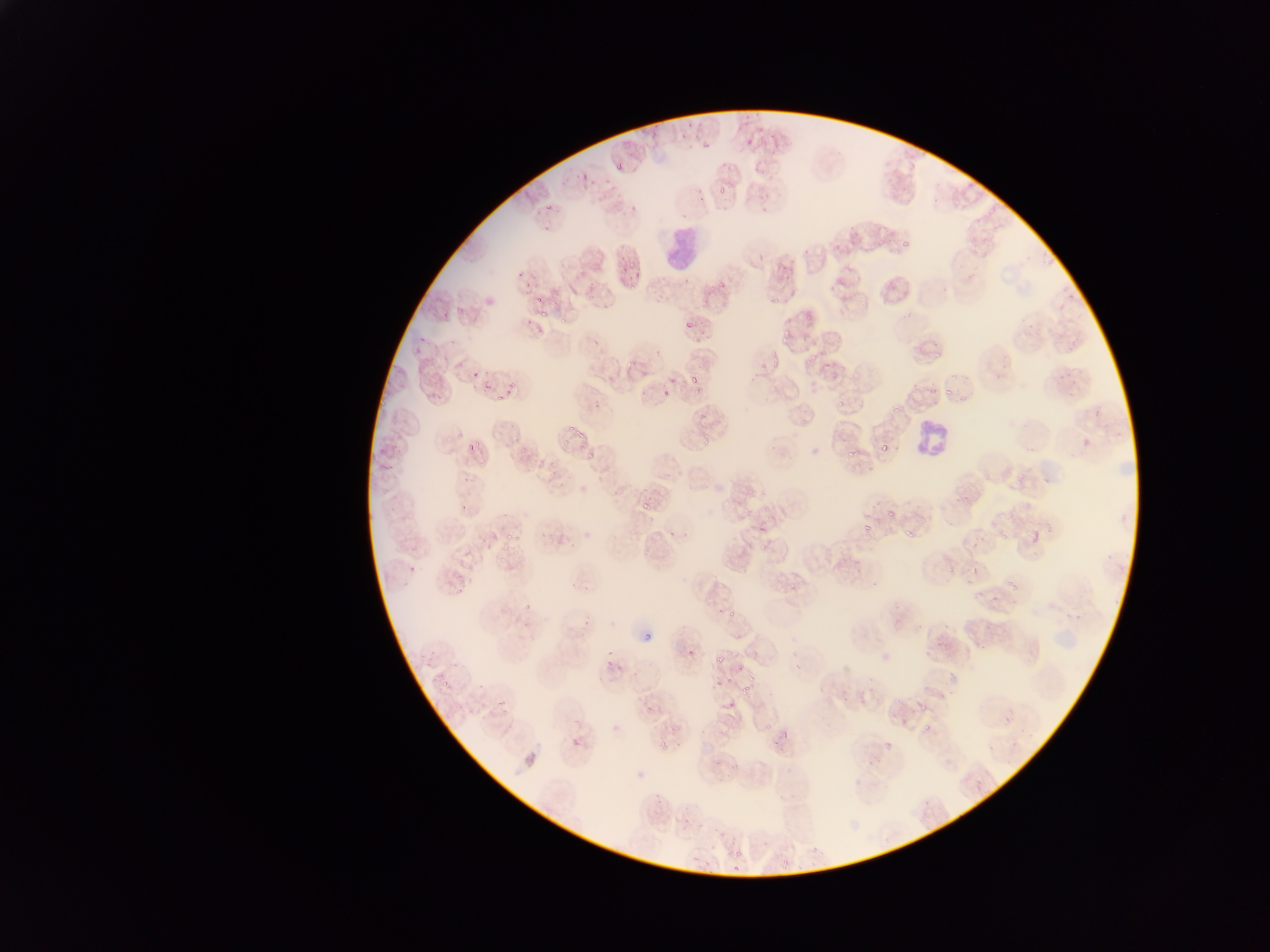

preparation: thin blood smear
image_size: 1270×952 pixels
field_of_view: single
plasmodium_parasite_locations: 'approximate bounding boxes as (left, top, right, bottom) in pixels: (744, 134, 756, 144), (697, 137, 711, 149), (759, 139, 768, 147), (615, 157, 630, 175), (580, 174, 592, 184), (718, 184, 730, 195), (544, 203, 555, 212), (899, 239, 912, 246), (832, 241, 841, 250), (615, 257, 629, 267), (633, 268, 646, 283), (618, 272, 631, 282), (525, 279, 537, 288), (628, 283, 636, 290), (719, 283, 726, 291), (585, 292, 598, 298), (771, 293, 785, 304), (533, 295, 545, 305), (539, 305, 551, 317), (804, 309, 815, 324), (559, 315, 567, 323), (682, 320, 694, 329), (767, 346, 778, 355), (803, 350, 819, 365), (626, 356, 636, 367), (772, 360, 780, 366), (758, 362, 766, 371), (469, 367, 482, 382), (831, 370, 839, 378), (688, 374, 700, 383), (668, 377, 676, 384), (508, 378, 517, 392), (942, 385, 950, 396), (694, 387, 702, 393), (662, 390, 671, 396), (836, 400, 844, 406), (891, 403, 902, 412), (699, 413, 710, 421), (800, 415, 810, 426), (566, 425, 575, 433), (575, 427, 587, 441), (467, 433, 482, 451), (560, 440, 571, 448), (701, 440, 712, 449), (519, 442, 531, 453), (879, 442, 889, 452), (846, 449, 855, 458), (588, 456, 600, 466), (534, 457, 551, 470), (1018, 469, 1027, 477), (748, 488, 755, 497), (760, 493, 771, 498), (952, 494, 970, 502), (640, 498, 653, 512), (461, 499, 474, 509), (760, 507, 771, 515), (883, 508, 896, 514), (758, 523, 767, 531), (862, 523, 872, 533), (1025, 526, 1046, 549), (669, 527, 683, 535), (902, 528, 912, 537), (506, 530, 523, 540), (1000, 531, 1009, 538), (761, 543, 772, 551), (497, 553, 508, 563), (972, 562, 980, 575), (407, 563, 419, 576), (1005, 579, 1013, 588), (791, 582, 800, 593), (990, 596, 999, 601), (523, 603, 533, 609), (728, 611, 736, 618), (641, 629, 655, 644), (733, 630, 741, 640), (685, 648, 695, 658), (926, 649, 933, 657), (714, 653, 726, 663), (601, 661, 609, 668), (732, 664, 742, 676), (441, 677, 450, 687), (711, 678, 722, 687), (742, 686, 754, 696), (726, 699, 735, 711), (498, 700, 508, 712), (918, 700, 924, 709), (764, 720, 779, 731), (923, 721, 930, 731), (571, 737, 582, 749), (656, 745, 669, 754), (969, 777, 987, 797), (735, 852, 744, 859), (782, 852, 794, 869) | approximate (x, y) pixel centers of objects too small to bound: (937, 353), (498, 399), (980, 594), (647, 711)'
capture: mobile-phone photograph through a microscope
leukocyte_locations: 'approximate bounding boxes as (left, top, right, bottom) in pixels: (660, 224, 703, 277), (908, 415, 955, 467)'
country: Ghana